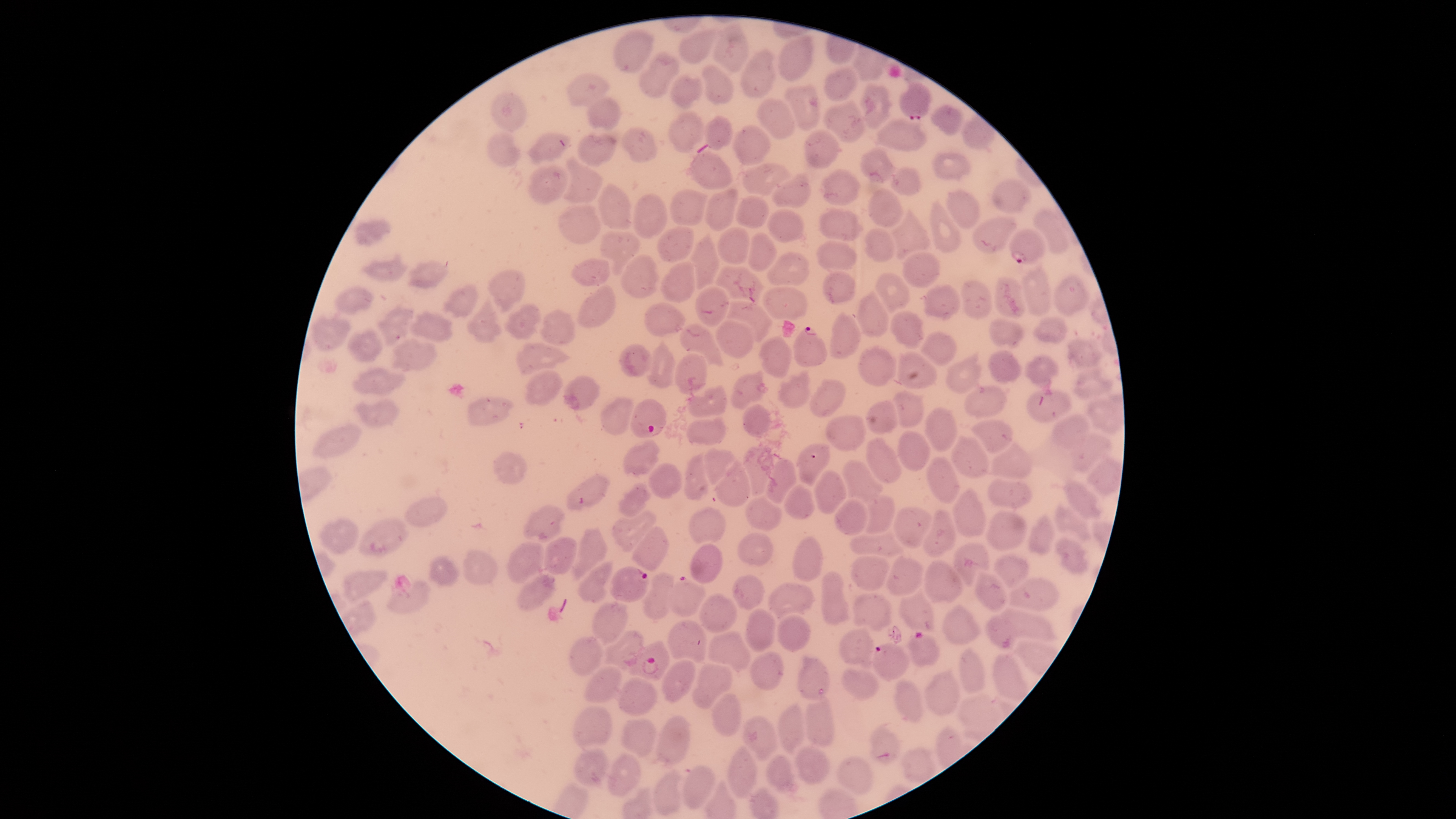

field of view = single
image size = 1456×819 pixels
species = Plasmodium falciparum
preparation = thin blood film
stain = Giemsa
uninfected RBCs = approximate bounding boxes, in pixels from the top-left corner: (left=710, top=21, right=749, bottom=73), (left=679, top=26, right=720, bottom=65), (left=612, top=29, right=655, bottom=73), (left=776, top=35, right=814, bottom=81), (left=739, top=46, right=778, bottom=99), (left=638, top=51, right=682, bottom=98), (left=701, top=64, right=736, bottom=105), (left=824, top=64, right=859, bottom=103), (left=564, top=72, right=612, bottom=107), (left=670, top=72, right=704, bottom=109), (left=783, top=83, right=821, bottom=131), (left=858, top=83, right=894, bottom=129), (left=488, top=90, right=527, bottom=133), (left=587, top=96, right=624, bottom=130), (left=756, top=98, right=796, bottom=139), (left=822, top=98, right=865, bottom=143), (left=930, top=105, right=964, bottom=136), (left=668, top=110, right=705, bottom=153), (left=704, top=114, right=734, bottom=152), (left=874, top=116, right=929, bottom=152), (left=731, top=124, right=771, bottom=165), (left=621, top=126, right=658, bottom=163), (left=486, top=129, right=521, bottom=168), (left=804, top=129, right=841, bottom=169), (left=525, top=131, right=572, bottom=164), (left=576, top=132, right=619, bottom=167), (left=858, top=145, right=898, bottom=184), (left=688, top=151, right=734, bottom=191), (left=932, top=151, right=971, bottom=181), (left=563, top=156, right=604, bottom=205), (left=740, top=161, right=794, bottom=196), (left=527, top=164, right=569, bottom=204), (left=889, top=166, right=921, bottom=195), (left=819, top=168, right=862, bottom=207), (left=771, top=170, right=813, bottom=208), (left=990, top=177, right=1032, bottom=214), (left=597, top=182, right=634, bottom=230), (left=867, top=186, right=903, bottom=229), (left=668, top=188, right=712, bottom=226), (left=704, top=188, right=739, bottom=231), (left=946, top=188, right=980, bottom=229), (left=633, top=193, right=668, bottom=240), (left=734, top=194, right=770, bottom=228), (left=928, top=198, right=961, bottom=254), (left=557, top=204, right=602, bottom=244), (left=816, top=205, right=864, bottom=242), (left=888, top=207, right=929, bottom=259), (left=766, top=208, right=804, bottom=242), (left=1034, top=209, right=1070, bottom=253), (left=972, top=214, right=1019, bottom=253), (left=354, top=217, right=392, bottom=247), (left=656, top=226, right=694, bottom=263), (left=716, top=226, right=750, bottom=264), (left=863, top=228, right=895, bottom=262), (left=599, top=230, right=644, bottom=277), (left=690, top=231, right=721, bottom=290), (left=747, top=232, right=778, bottom=271), (left=814, top=240, right=857, bottom=270), (left=765, top=250, right=809, bottom=287), (left=901, top=250, right=941, bottom=289), (left=360, top=251, right=409, bottom=282), (left=620, top=254, right=660, bottom=300), (left=569, top=258, right=609, bottom=288), (left=407, top=259, right=450, bottom=289), (left=660, top=260, right=696, bottom=302), (left=1018, top=262, right=1052, bottom=316), (left=715, top=266, right=764, bottom=302), (left=486, top=269, right=526, bottom=313), (left=821, top=270, right=857, bottom=306), (left=875, top=271, right=911, bottom=313), (left=1053, top=274, right=1091, bottom=318), (left=994, top=277, right=1027, bottom=318), (left=960, top=279, right=994, bottom=319), (left=577, top=283, right=618, bottom=329), (left=441, top=284, right=480, bottom=319), (left=921, top=284, right=961, bottom=321), (left=334, top=285, right=375, bottom=317), (left=694, top=285, right=729, bottom=327), (left=761, top=286, right=808, bottom=320), (left=855, top=289, right=890, bottom=338), (left=466, top=294, right=502, bottom=344), (left=726, top=300, right=775, bottom=341), (left=644, top=301, right=687, bottom=338), (left=502, top=302, right=542, bottom=340), (left=377, top=304, right=415, bottom=349), (left=409, top=307, right=454, bottom=343), (left=539, top=308, right=576, bottom=348), (left=828, top=310, right=862, bottom=360), (left=889, top=310, right=927, bottom=348), (left=309, top=314, right=353, bottom=352), (left=1033, top=314, right=1069, bottom=345), (left=986, top=315, right=1026, bottom=348), (left=714, top=318, right=755, bottom=360), (left=680, top=323, right=725, bottom=367), (left=347, top=328, right=384, bottom=363), (left=918, top=330, right=958, bottom=367), (left=759, top=335, right=792, bottom=379), (left=391, top=337, right=440, bottom=372), (left=1066, top=338, right=1106, bottom=370), (left=647, top=339, right=676, bottom=387), (left=515, top=341, right=574, bottom=376), (left=617, top=343, right=652, bottom=378), (left=858, top=344, right=898, bottom=387), (left=945, top=348, right=983, bottom=394), (left=988, top=349, right=1022, bottom=384), (left=896, top=350, right=939, bottom=389), (left=675, top=353, right=707, bottom=396), (left=1023, top=354, right=1059, bottom=386), (left=1072, top=365, right=1115, bottom=402), (left=352, top=367, right=407, bottom=396), (left=523, top=369, right=563, bottom=407), (left=729, top=369, right=769, bottom=411), (left=776, top=369, right=812, bottom=408), (left=561, top=375, right=600, bottom=411), (left=808, top=377, right=847, bottom=418), (left=964, top=383, right=1008, bottom=418), (left=687, top=384, right=728, bottom=418), (left=1026, top=388, right=1073, bottom=423), (left=892, top=389, right=924, bottom=428), (left=1083, top=390, right=1124, bottom=436), (left=352, top=396, right=400, bottom=429), (left=466, top=396, right=515, bottom=426), (left=599, top=396, right=634, bottom=436), (left=742, top=404, right=772, bottom=438), (left=923, top=407, right=958, bottom=452), (left=1049, top=413, right=1093, bottom=450), (left=824, top=414, right=865, bottom=452), (left=684, top=415, right=728, bottom=446), (left=969, top=419, right=1013, bottom=453), (left=311, top=421, right=363, bottom=458), (left=896, top=429, right=930, bottom=472), (left=1067, top=432, right=1113, bottom=474), (left=950, top=434, right=990, bottom=479), (left=865, top=436, right=903, bottom=484), (left=621, top=439, right=660, bottom=479), (left=988, top=440, right=1034, bottom=480), (left=795, top=442, right=831, bottom=489), (left=741, top=446, right=773, bottom=497), (left=684, top=450, right=711, bottom=501), (left=494, top=451, right=527, bottom=486), (left=926, top=455, right=960, bottom=503), (left=1085, top=455, right=1124, bottom=498), (left=765, top=456, right=798, bottom=505), (left=715, top=457, right=749, bottom=507), (left=841, top=460, right=883, bottom=504), (left=649, top=462, right=682, bottom=499), (left=814, top=469, right=847, bottom=516), (left=566, top=472, right=612, bottom=510), (left=1062, top=476, right=1104, bottom=520), (left=987, top=478, right=1032, bottom=508), (left=616, top=482, right=652, bottom=519), (left=783, top=484, right=815, bottom=520), (left=951, top=487, right=986, bottom=537), (left=863, top=493, right=896, bottom=534), (left=745, top=494, right=782, bottom=532), (left=404, top=495, right=450, bottom=528), (left=833, top=499, right=869, bottom=536), (left=523, top=504, right=567, bottom=545), (left=891, top=504, right=933, bottom=548), (left=1053, top=504, right=1093, bottom=541), (left=689, top=506, right=726, bottom=545), (left=921, top=508, right=957, bottom=560), (left=609, top=510, right=657, bottom=554), (left=984, top=510, right=1028, bottom=551), (left=1028, top=513, right=1055, bottom=556), (left=356, top=516, right=409, bottom=554), (left=318, top=517, right=359, bottom=554), (left=569, top=526, right=609, bottom=582), (left=631, top=527, right=669, bottom=572), (left=849, top=531, right=904, bottom=559), (left=736, top=532, right=774, bottom=566), (left=543, top=535, right=578, bottom=575), (left=792, top=535, right=824, bottom=582), (left=1054, top=536, right=1089, bottom=575), (left=953, top=540, right=991, bottom=587), (left=506, top=541, right=546, bottom=584), (left=690, top=543, right=723, bottom=584), (left=461, top=548, right=499, bottom=586), (left=426, top=553, right=461, bottom=587), (left=994, top=553, right=1029, bottom=588), (left=849, top=555, right=890, bottom=592), (left=884, top=555, right=925, bottom=599), (left=575, top=559, right=615, bottom=604), (left=923, top=559, right=964, bottom=604), (left=341, top=569, right=389, bottom=604), (left=821, top=570, right=852, bottom=628), (left=975, top=570, right=1007, bottom=610), (left=640, top=572, right=675, bottom=621), (left=515, top=573, right=559, bottom=612), (left=732, top=573, right=766, bottom=611), (left=1009, top=578, right=1061, bottom=612), (left=385, top=580, right=431, bottom=614), (left=767, top=582, right=815, bottom=623), (left=897, top=587, right=936, bottom=632), (left=698, top=592, right=739, bottom=634), (left=852, top=592, right=893, bottom=635), (left=591, top=600, right=629, bottom=643), (left=942, top=604, right=982, bottom=645), (left=744, top=607, right=776, bottom=654), (left=1000, top=609, right=1059, bottom=641), (left=775, top=614, right=812, bottom=653), (left=985, top=614, right=1016, bottom=650), (left=666, top=620, right=707, bottom=663), (left=838, top=627, right=875, bottom=666), (left=603, top=630, right=645, bottom=666), (left=705, top=632, right=751, bottom=672), (left=567, top=636, right=605, bottom=677), (left=748, top=651, right=785, bottom=692), (left=993, top=652, right=1029, bottom=703), (left=796, top=654, right=830, bottom=700), (left=659, top=658, right=696, bottom=705), (left=691, top=663, right=733, bottom=710), (left=584, top=665, right=624, bottom=704), (left=840, top=667, right=881, bottom=701), (left=924, top=667, right=961, bottom=716), (left=617, top=677, right=660, bottom=717), (left=892, top=678, right=924, bottom=723), (left=711, top=692, right=742, bottom=737), (left=956, top=693, right=1001, bottom=741), (left=804, top=696, right=833, bottom=748), (left=776, top=701, right=806, bottom=756), (left=571, top=706, right=613, bottom=752), (left=655, top=716, right=691, bottom=769), (left=742, top=716, right=778, bottom=761), (left=621, top=718, right=657, bottom=759), (left=869, top=725, right=902, bottom=764), (left=792, top=743, right=833, bottom=785), (left=727, top=744, right=759, bottom=798), (left=901, top=745, right=936, bottom=785), (left=574, top=748, right=610, bottom=790), (left=606, top=752, right=642, bottom=796), (left=765, top=754, right=801, bottom=795), (left=835, top=756, right=874, bottom=793), (left=682, top=764, right=717, bottom=809), (left=652, top=768, right=683, bottom=816)
visible region = circular
capture = smartphone photograph through the microscope eyepiece
presence = malaria parasites identified
parasitized RBCs = approximate bounding boxes, in pixels from the top-left corner: (left=900, top=79, right=933, bottom=120), (left=1009, top=228, right=1046, bottom=264), (left=794, top=326, right=828, bottom=366), (left=630, top=398, right=666, bottom=437), (left=609, top=566, right=649, bottom=602), (left=669, top=575, right=706, bottom=616), (left=907, top=631, right=939, bottom=667), (left=616, top=640, right=670, bottom=681), (left=872, top=642, right=909, bottom=681)